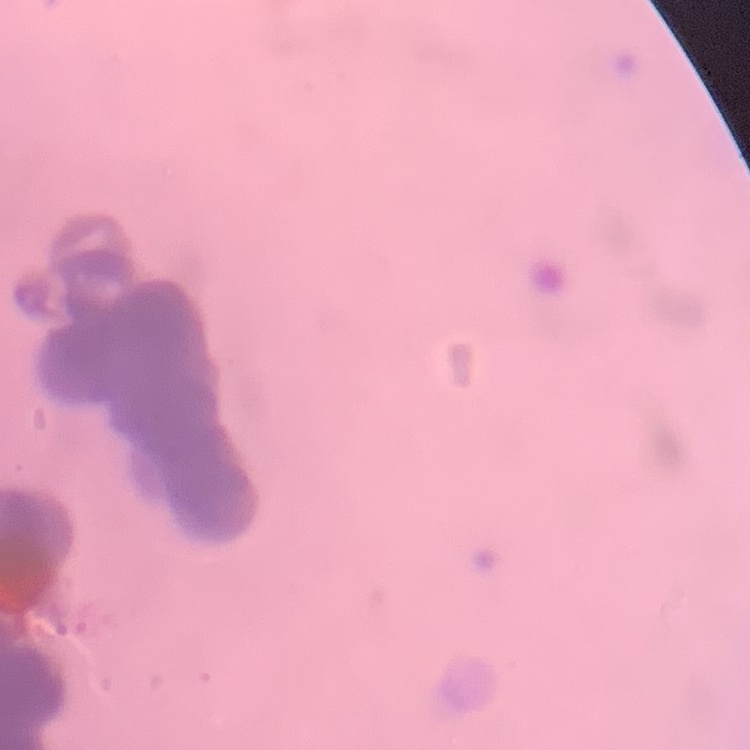

The red blood cells show rouleaux formation. Stained with either Field's or Giemsa. Square crop of a larger photomicrograph. Thin blood smear.